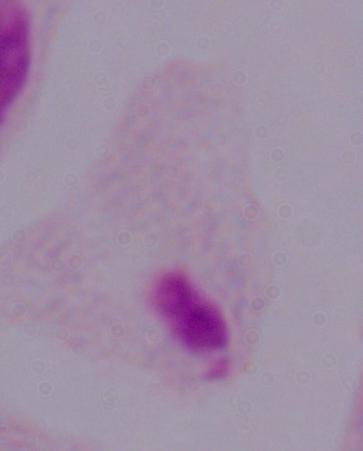
magnification: 1000x
modality: photomicrograph
identification: trichomonad